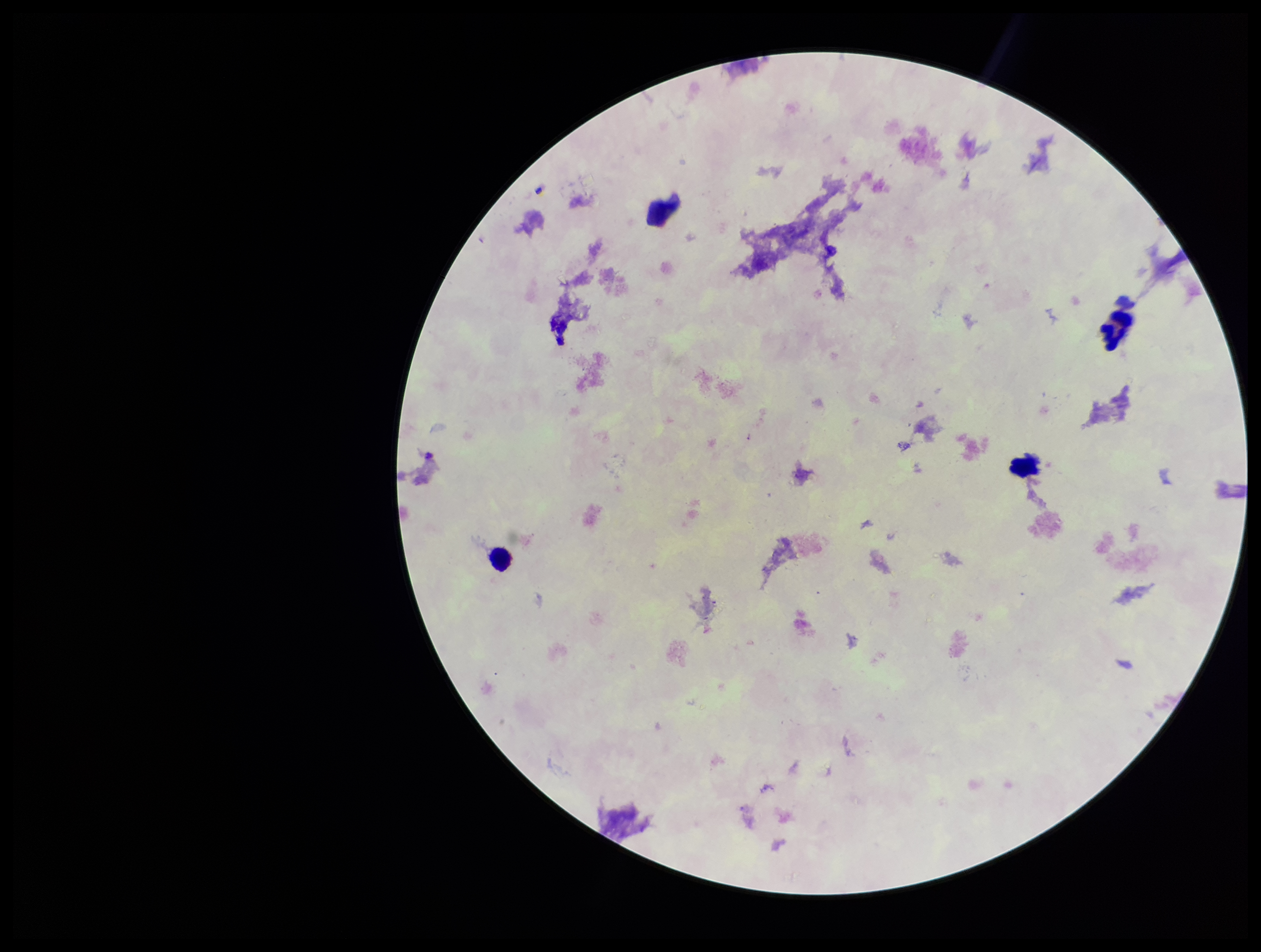

preparation = thick smear
leukocyte count = 4
image size = 1261×952 pixels
Plasmodium parasites = none identified
capture = smartphone photograph through the microscope eyepiece
field of view = one from this slide
stain = Giemsa
parasite count = 0
patient malaria status = negative